Classify this cell by malaria status.
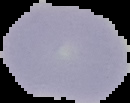
Uninfected.

preparation = thin blood smear
image size = 130×103 pixels
image type = cell region segmented out of the field of view; surrounding area masked to black